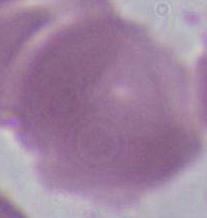

Captured at 1000x magnification. A red blood cell is shown. Photomicrograph.